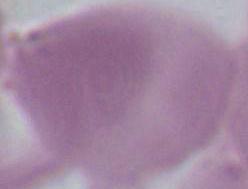

modality: photomicrograph
magnification: 1000x
identification: red blood cell